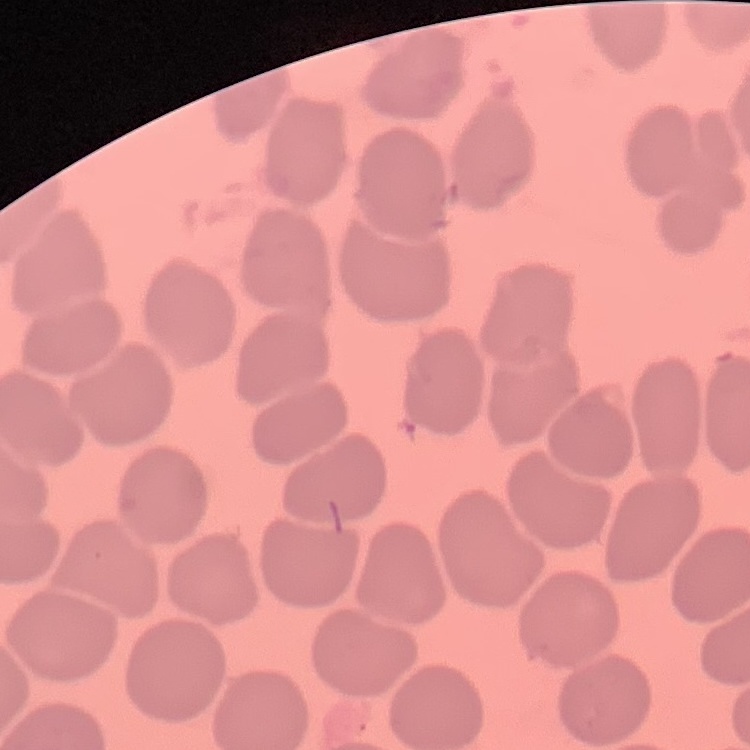
Summary:
  - Erythrocyte morphology: no rouleaux formation
  - Preparation: thin blood film
  - Image type: one tile cut from a larger photomicrograph
  - Stain: Field's or Giemsa